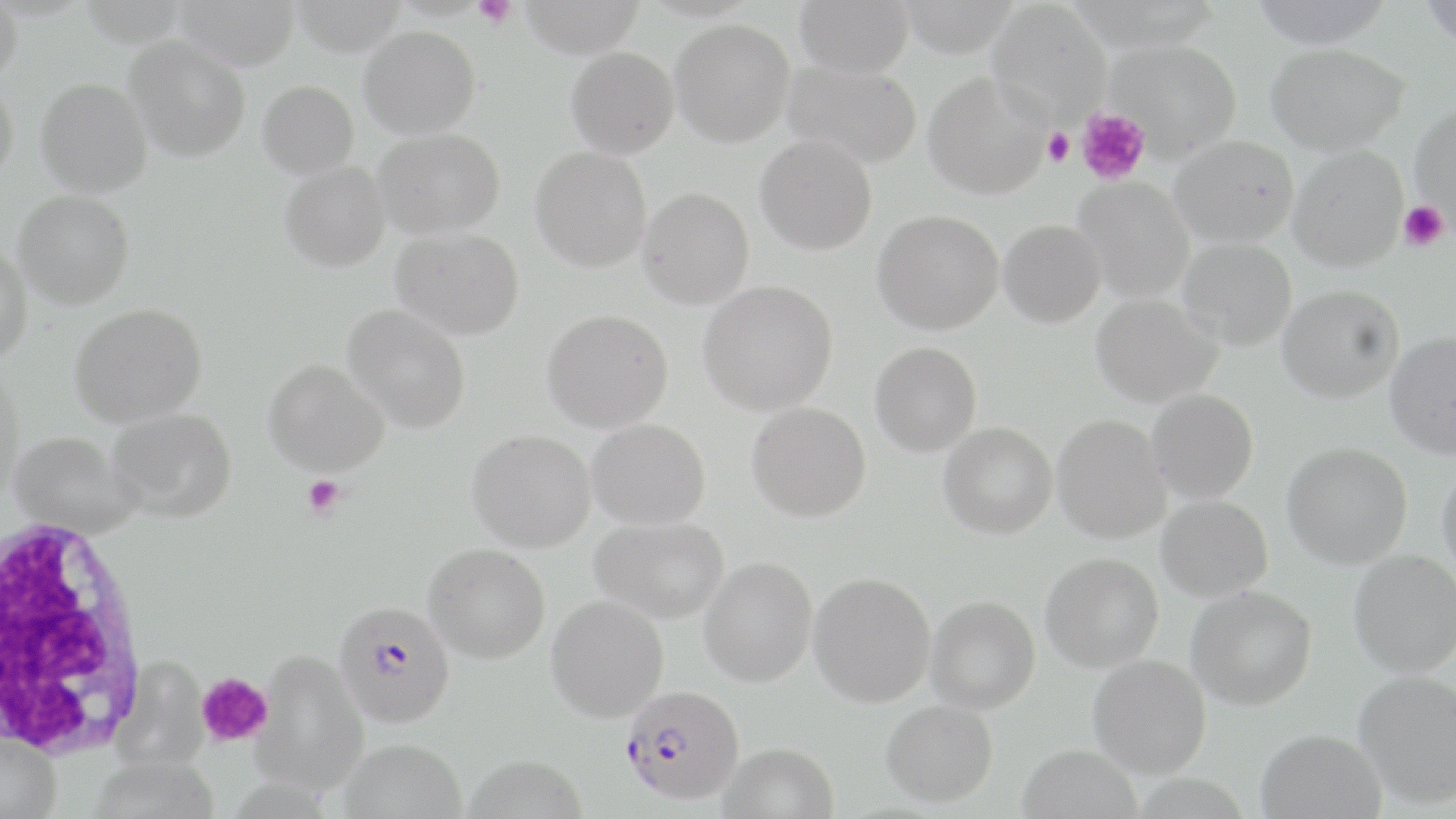
Approximate bounding boxes as (x1,y1)-(x2,y2) corner pairs in pixels. Platelet locations: (474,0)-(517,28), (1076,108)-(1150,186), (1042,127)-(1075,166), (1398,200)-(1450,251), (302,475)-(346,518), (196,671)-(274,748). Plasmodium falciparum-infected red blood cell locations: (335,601)-(456,728), (620,685)-(746,806). White blood cell locations: (1,516)-(152,760). Uninfected red blood cell locations: (0,0)-(23,85), (174,0)-(300,71), (519,0)-(646,58), (794,0)-(913,78), (1248,0)-(1395,49), (1419,0)-(1455,48), (986,2)-(1112,126), (670,19)-(795,146), (358,26)-(481,138), (125,36)-(250,162), (1106,39)-(1242,158), (1265,43)-(1409,154), (566,46)-(679,158), (782,60)-(922,169), (923,71)-(1050,200), (36,77)-(152,198), (0,78)-(19,183), (257,80)-(359,180), (1410,103)-(1456,223), (373,128)-(504,239), (754,135)-(877,255), (1169,135)-(1299,246), (1288,145)-(1408,271), (531,146)-(651,272), (279,162)-(390,272), (1073,177)-(1195,303), (637,188)-(754,309), (13,190)-(134,309), (872,209)-(1004,335), (998,219)-(1106,328), (391,228)-(524,340), (1178,238)-(1297,350), (0,243)-(33,364), (698,280)-(837,416), (1277,284)-(1404,403), (1091,294)-(1222,408), (69,303)-(207,427), (344,305)-(470,433), (542,309)-(673,432), (1384,331)-(1456,459), (870,342)-(982,456), (263,359)-(389,476), (0,367)-(25,503), (1146,389)-(1259,503), (746,401)-(871,522), (109,408)-(237,521), (1052,415)-(1171,544), (587,418)-(711,529), (938,423)-(1057,539), (467,430)-(596,552), (9,431)-(143,538), (1282,441)-(1412,569), (1436,462)-(1456,581), (1156,495)-(1273,602), (590,516)-(729,624), (423,543)-(550,663), (1349,550)-(1456,677), (1040,553)-(1163,672), (699,556)-(817,687), (808,571)-(936,707), (1186,586)-(1317,710), (545,595)-(669,722), (926,595)-(1040,713), (253,650)-(369,797), (1088,654)-(1211,778), (113,656)-(208,771), (1353,670)-(1456,808), (881,699)-(998,807), (1256,728)-(1386,819), (0,730)-(61,819), (338,738)-(468,819), (718,742)-(838,819), (1017,743)-(1144,819). Slide-level diagnosis: Plasmodium falciparum. Thin blood smear. Light microscopy. One field of a larger specimen. May-Grünwald-Giemsa-stained preparation. Image is 1456×819 pixels. 1000x magnification.